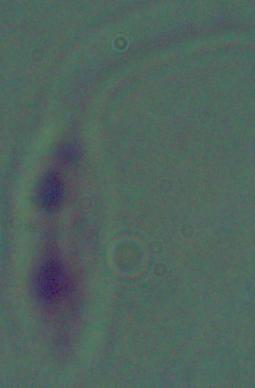
Micrograph. A Leishmania parasite is shown. Captured at 1000x magnification.